State the blood parasite species.
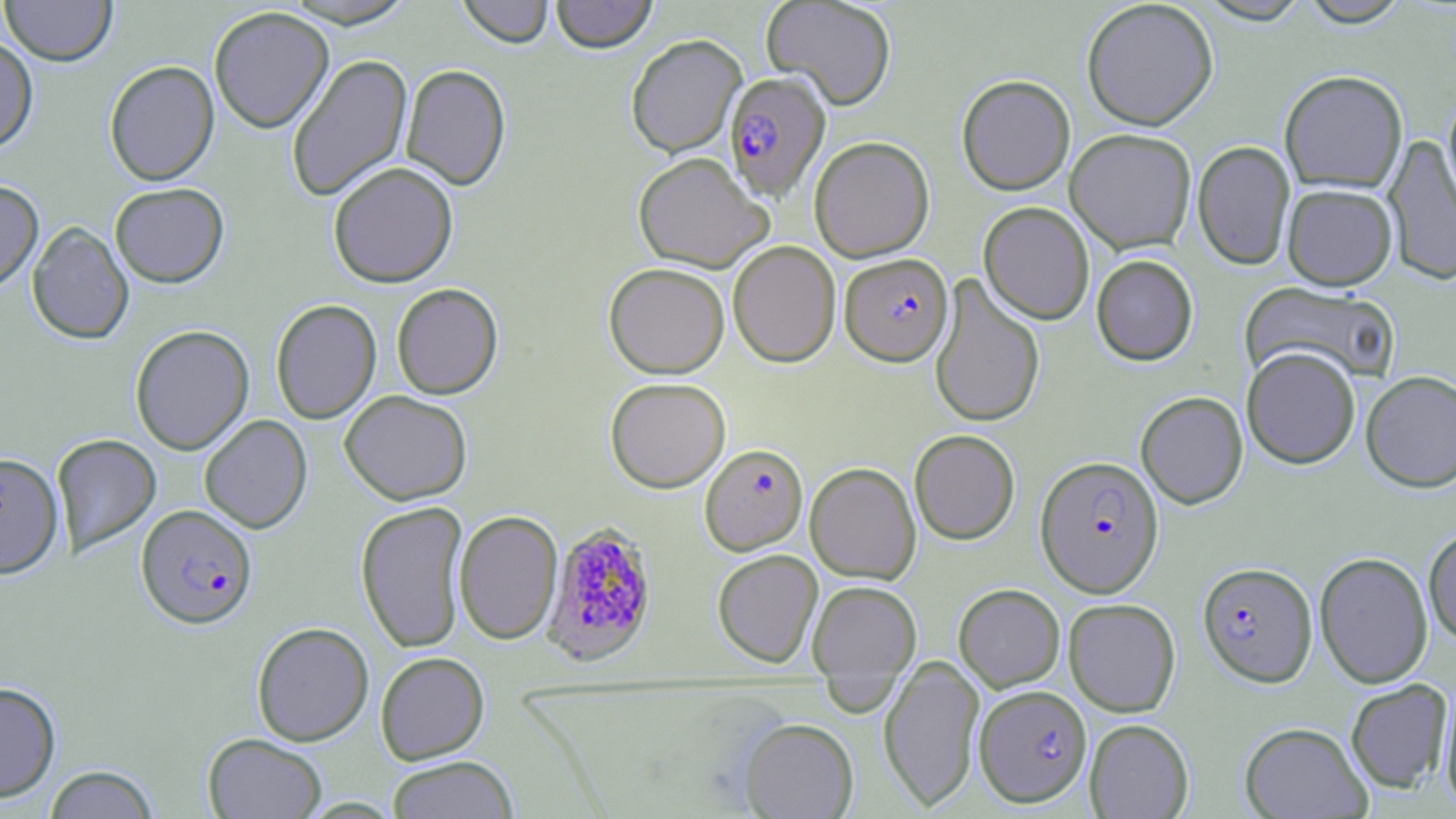

Plasmodium falciparum.

Approximate bounding boxes as [x1, y1, x2, y2] in pixels. Uninfected red blood cell locations: [1, 0, 117, 65], [278, 0, 420, 28], [456, 0, 554, 48], [551, 0, 658, 53], [761, 0, 897, 110], [1081, 0, 1219, 130], [1194, 0, 1314, 25], [1296, 0, 1414, 27], [208, 6, 334, 133], [625, 34, 747, 158], [0, 36, 38, 153], [286, 53, 413, 203], [104, 60, 219, 186], [401, 63, 511, 190], [1279, 70, 1407, 194], [956, 74, 1075, 195], [1441, 88, 1456, 218], [1065, 128, 1197, 254], [1383, 134, 1456, 286], [809, 136, 934, 262], [1192, 141, 1295, 270], [633, 152, 773, 273], [328, 161, 458, 288], [0, 179, 43, 292], [110, 182, 229, 287], [1282, 183, 1397, 290], [978, 202, 1094, 324], [27, 222, 134, 344], [728, 240, 841, 368], [1091, 255, 1198, 366], [603, 263, 730, 378], [929, 275, 1045, 429], [1240, 280, 1402, 387], [391, 283, 503, 399], [270, 299, 382, 424], [130, 325, 254, 454], [1242, 346, 1360, 468], [1360, 371, 1456, 492], [605, 377, 731, 493], [339, 390, 473, 505], [1136, 391, 1248, 509], [199, 414, 312, 533], [909, 429, 1020, 544], [52, 434, 161, 556], [0, 451, 63, 580], [805, 461, 921, 584], [355, 500, 469, 653], [454, 510, 563, 645], [1423, 526, 1456, 648], [712, 549, 823, 668], [1315, 551, 1433, 689], [807, 579, 921, 697], [953, 583, 1065, 692], [1064, 598, 1181, 717], [252, 622, 373, 746], [376, 651, 489, 764], [879, 653, 984, 812], [1345, 679, 1453, 794], [0, 681, 61, 803], [1439, 684, 1456, 813], [738, 717, 859, 818], [1084, 718, 1194, 818], [1239, 722, 1372, 818], [203, 733, 327, 818], [386, 756, 518, 819], [43, 764, 160, 819]. Plasmodium falciparum-infected red blood cell locations: [724, 72, 830, 201], [840, 253, 953, 366], [700, 443, 808, 555], [1035, 456, 1163, 597], [136, 504, 257, 628], [541, 521, 658, 667], [1198, 561, 1317, 687], [975, 684, 1092, 806]. Thin blood smear. One field of a larger specimen. Captured at 1000x magnification. Image is 1456×819 pixels. Light microscopy. May-Grünwald-Giemsa stain.